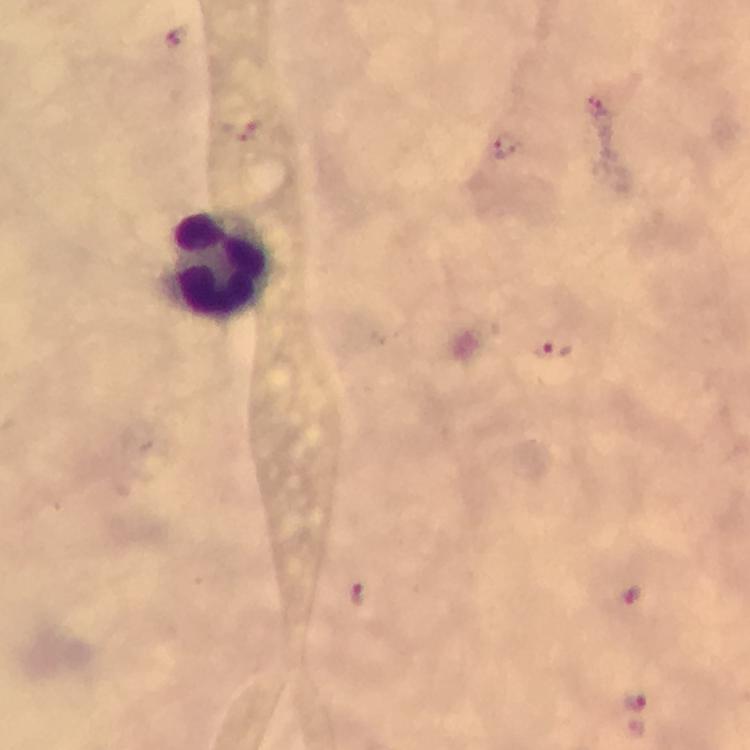

Approximate centers as {x, y} in pixels. Leukocyte locations: {219, 262}. Plasmodium parasite locations: {174, 36}, {597, 104}, {506, 145}, {554, 348}, {356, 595}, {634, 596}, {635, 702}. Thick blood film. Giemsa stain. Image is 750×750 pixels. Immersion oil applied. Photographed through the microscope with a smartphone camera. From a malaria diagnostic workup. 100x magnification. A crop from one field of view.